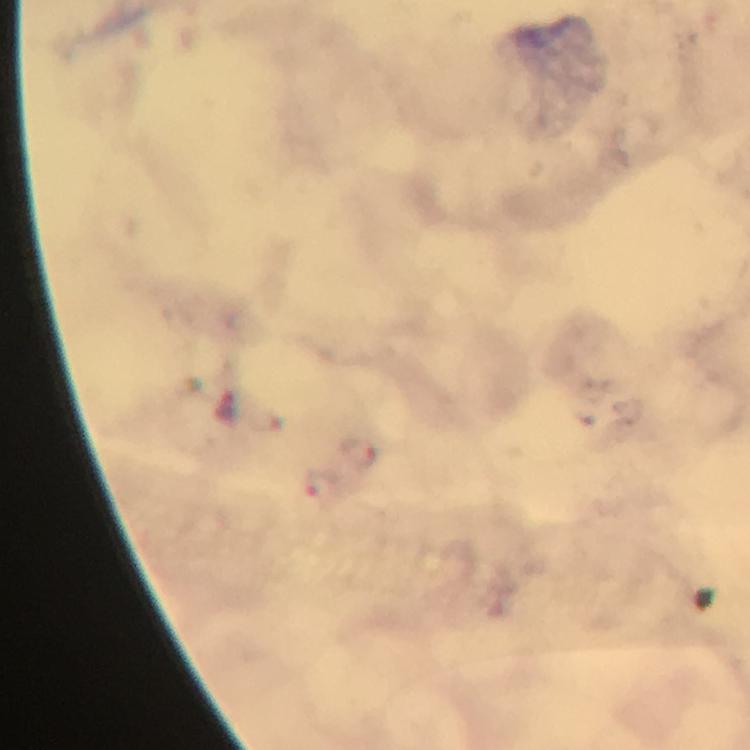
Approximate centers as [x, y] in pixels.
Summary:
  - Plasmodium parasite locations: [359, 455], [322, 486]
  - Capture: smartphone camera through the microscope
  - Context: from a malaria diagnostic workup
  - Magnification: 100x
  - Image size: 750×750 pixels
  - Stain: Giemsa
  - Immersion oil: used
  - Preparation: thick smear
  - Cropped from: a single field of view